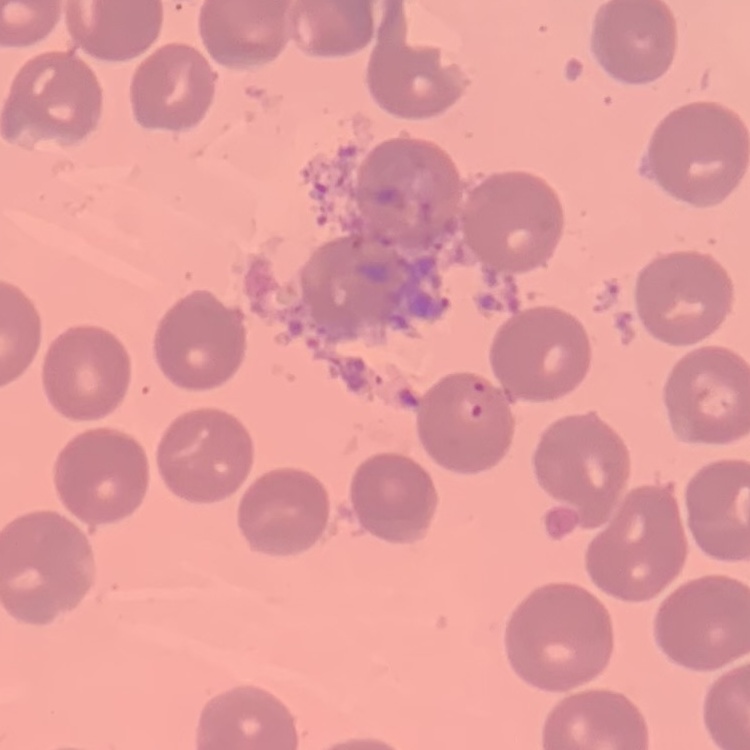
Summary:
  - Erythrocyte morphology: no rouleaux formation
  - Image type: square crop of a larger photomicrograph
  - Preparation: thin blood film
  - Stain: Field's or Giemsa